Outline each Plasmodium falciparum-infected red blood cell.
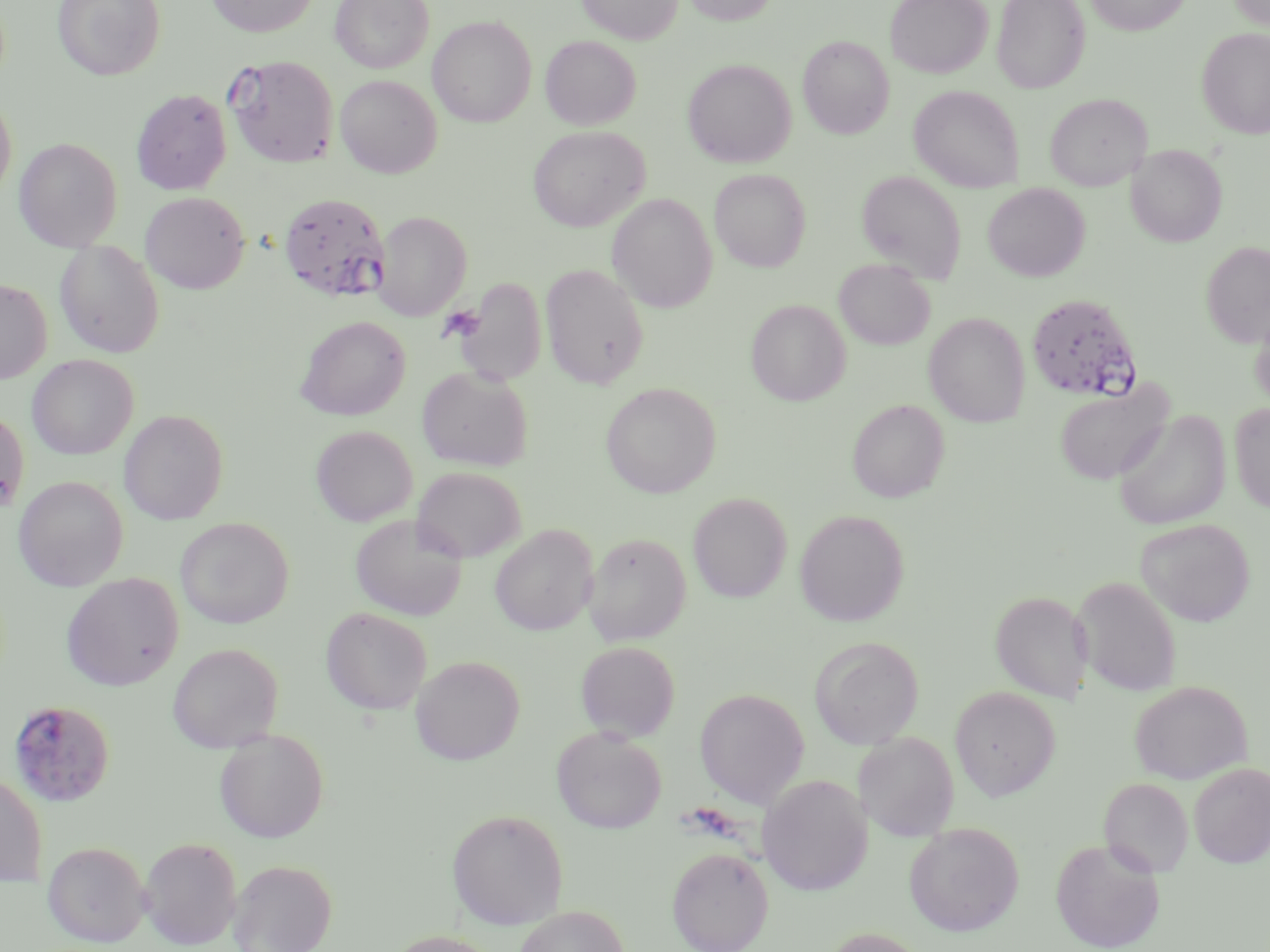
Approximate bounding boxes as (x1,y1)-(x2,y2) corner pairs in pixels.
Plasmodium falciparum-infected red blood cells: (225,55)-(339,168), (279,192)-(390,302), (1025,293)-(1143,402), (8,699)-(115,808).

slide_level_diagnosis: Plasmodium falciparum
stain: May-Grünwald-Giemsa
image_size: 1270×952 pixels
preparation: thin blood smear
uninfected_red_blood_cell_locations: 'approximate bounding boxes as (x1,y1)-(x2,y2) corner pairs in pixels: (52,0)-(166,81), (205,0)-(319,37), (329,0)-(433,73), (577,0)-(682,44), (680,0)-(780,25), (885,0)-(993,78), (992,0)-(1090,93), (1085,0)-(1192,35), (1227,0)-(1270,30), (428,15)-(536,128), (1197,27)-(1270,139), (540,35)-(641,130), (797,35)-(893,139), (683,58)-(797,168), (335,74)-(442,178), (908,85)-(1025,192), (131,89)-(232,195), (0,91)-(17,202), (1045,93)-(1150,191), (527,125)-(649,232), (14,137)-(123,251), (1127,144)-(1227,247), (710,168)-(811,271), (856,169)-(967,284), (983,183)-(1090,281), (140,191)-(250,294), (606,193)-(717,313), (373,211)-(471,321), (54,241)-(164,358), (1200,241)-(1270,348), (834,259)-(935,349), (540,263)-(649,389), (452,276)-(547,385), (0,279)-(51,384), (745,299)-(851,406), (1250,310)-(1270,412), (924,312)-(1030,427), (296,316)-(410,421), (27,355)-(138,460), (416,366)-(533,471), (1054,380)-(1174,485), (601,382)-(720,498), (847,399)-(949,503), (1229,403)-(1270,514), (0,405)-(29,519), (119,409)-(229,525), (1112,410)-(1231,531), (311,425)-(417,526), (412,466)-(526,562), (14,475)-(128,591), (688,492)-(792,602), (688,499)-(909,612), (794,509)-(910,626), (350,515)-(466,621), (175,517)-(294,629), (1135,518)-(1255,627), (490,525)-(598,636), (583,532)-(691,645), (61,573)-(183,691), (1073,575)-(1183,697), (991,591)-(1092,703), (321,607)-(432,715), (809,636)-(924,749), (575,641)-(680,741), (168,643)-(283,752), (411,655)-(525,765), (1129,680)-(1253,785), (949,685)-(1061,801), (694,688)-(810,808), (551,726)-(667,833), (214,728)-(329,843), (854,732)-(959,840), (1188,762)-(1270,867), (0,772)-(48,886), (757,774)-(873,896), (1099,777)-(1193,877), (446,808)-(568,928), (904,823)-(1024,936), (138,836)-(243,949), (1050,838)-(1165,952), (42,841)-(151,947), (667,847)-(773,951), (227,859)-(337,952), (513,906)-(630,952), (819,928)-(933,952), (384,930)-(502,952)'
modality: light microscopy
magnification: 1000x
field_of_view: single